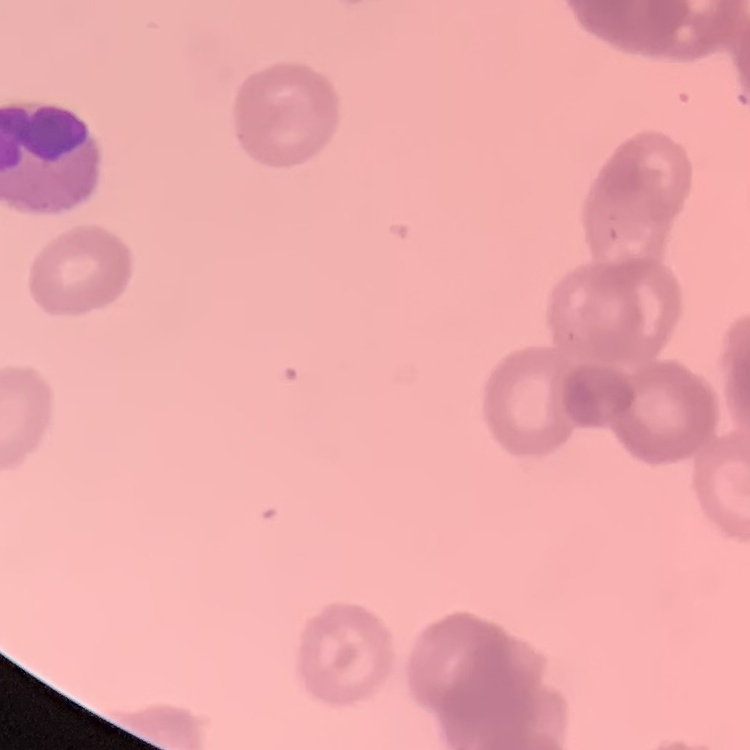
Summary:
  - Red blood cell morphology: rouleaux formation
  - Stain: Field's or Giemsa
  - Image type: one tile cut from a larger photomicrograph
  - Preparation: thin peripheral smear